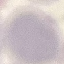

result: no malaria parasites seen
capture: smartphone through the microscope eyepiece
stain: Giemsa
preparation: thin blood smear
image_type: cell patch, automatically extracted from a larger field of view and resized to 64 × 64 pixels